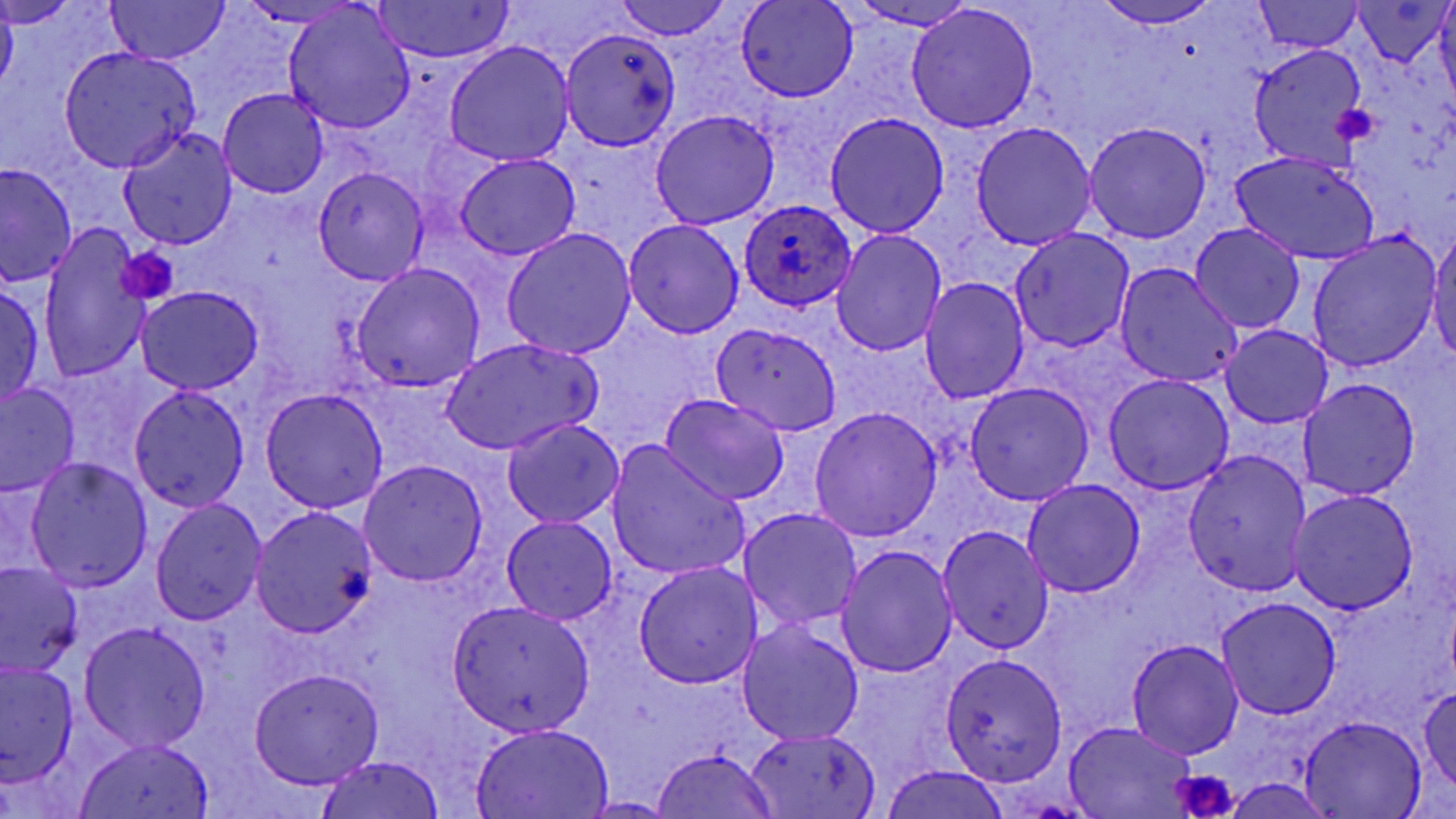

Approximate bounding boxes as named x1/y1/x2/y2 corners in pixels. Platelet locations: (x1=1332, y1=101, x2=1381, y2=144), (x1=118, y1=245, x2=179, y2=303), (x1=1171, y1=768, x2=1241, y2=819). Uninfected red blood cell locations: (x1=0, y1=0, x2=76, y2=28), (x1=105, y1=0, x2=229, y2=63), (x1=614, y1=0, x2=727, y2=41), (x1=736, y1=0, x2=857, y2=102), (x1=1094, y1=0, x2=1224, y2=28), (x1=1358, y1=0, x2=1452, y2=68), (x1=238, y1=1, x2=366, y2=27), (x1=372, y1=1, x2=515, y2=63), (x1=844, y1=1, x2=982, y2=31), (x1=1258, y1=1, x2=1362, y2=53), (x1=1, y1=3, x2=18, y2=94), (x1=283, y1=3, x2=417, y2=135), (x1=905, y1=6, x2=1040, y2=134), (x1=560, y1=27, x2=682, y2=150), (x1=444, y1=41, x2=575, y2=167), (x1=1249, y1=45, x2=1367, y2=166), (x1=57, y1=47, x2=203, y2=172), (x1=218, y1=88, x2=328, y2=198), (x1=650, y1=108, x2=780, y2=230), (x1=824, y1=114, x2=949, y2=237), (x1=970, y1=121, x2=1097, y2=250), (x1=1085, y1=121, x2=1213, y2=243), (x1=118, y1=126, x2=237, y2=250), (x1=1229, y1=151, x2=1381, y2=265), (x1=455, y1=153, x2=582, y2=259), (x1=1, y1=163, x2=79, y2=288), (x1=313, y1=166, x2=429, y2=286), (x1=623, y1=217, x2=746, y2=339), (x1=1190, y1=222, x2=1306, y2=333), (x1=1427, y1=223, x2=1456, y2=363), (x1=38, y1=225, x2=152, y2=386), (x1=501, y1=228, x2=637, y2=360), (x1=1010, y1=228, x2=1136, y2=353), (x1=833, y1=229, x2=945, y2=358), (x1=1306, y1=234, x2=1441, y2=372), (x1=352, y1=262, x2=484, y2=390), (x1=1114, y1=264, x2=1244, y2=388), (x1=919, y1=279, x2=1029, y2=405), (x1=0, y1=283, x2=45, y2=407), (x1=137, y1=287, x2=265, y2=395), (x1=709, y1=323, x2=844, y2=438), (x1=1220, y1=325, x2=1332, y2=428), (x1=441, y1=337, x2=600, y2=454), (x1=1104, y1=374, x2=1234, y2=493), (x1=1299, y1=378, x2=1421, y2=500), (x1=965, y1=381, x2=1095, y2=504), (x1=1, y1=384, x2=81, y2=498), (x1=129, y1=384, x2=250, y2=512), (x1=260, y1=389, x2=389, y2=514), (x1=659, y1=394, x2=789, y2=508), (x1=810, y1=407, x2=942, y2=540), (x1=501, y1=417, x2=624, y2=528), (x1=607, y1=443, x2=751, y2=583), (x1=1182, y1=449, x2=1313, y2=597), (x1=24, y1=457, x2=153, y2=592), (x1=359, y1=459, x2=488, y2=588), (x1=1021, y1=480, x2=1146, y2=599), (x1=1288, y1=489, x2=1419, y2=615), (x1=151, y1=498, x2=267, y2=625), (x1=250, y1=504, x2=379, y2=637), (x1=739, y1=508, x2=861, y2=631), (x1=500, y1=515, x2=618, y2=624), (x1=937, y1=525, x2=1054, y2=653), (x1=837, y1=545, x2=958, y2=677), (x1=0, y1=562, x2=82, y2=678), (x1=633, y1=562, x2=764, y2=690), (x1=1216, y1=597, x2=1342, y2=717), (x1=447, y1=600, x2=596, y2=736), (x1=738, y1=621, x2=864, y2=746), (x1=78, y1=622, x2=212, y2=753), (x1=1126, y1=639, x2=1244, y2=759), (x1=940, y1=655, x2=1066, y2=787), (x1=0, y1=661, x2=77, y2=788), (x1=249, y1=668, x2=384, y2=788), (x1=1417, y1=688, x2=1456, y2=793), (x1=1300, y1=716, x2=1428, y2=817), (x1=469, y1=722, x2=614, y2=818), (x1=1064, y1=722, x2=1198, y2=816), (x1=741, y1=727, x2=883, y2=817), (x1=73, y1=738, x2=217, y2=819), (x1=651, y1=748, x2=780, y2=818), (x1=312, y1=754, x2=448, y2=819), (x1=881, y1=765, x2=1014, y2=819), (x1=1224, y1=777, x2=1335, y2=817), (x1=579, y1=797, x2=682, y2=816). Plasmodium ovale-infected red blood cell locations: (x1=739, y1=200, x2=856, y2=311). Slide-level diagnosis: Plasmodium ovale. Captured at 1000x magnification. Image is 1456×819 pixels. May-Grünwald-Giemsa stain. Optical microscopy. One field of a larger specimen. Thin blood smear.